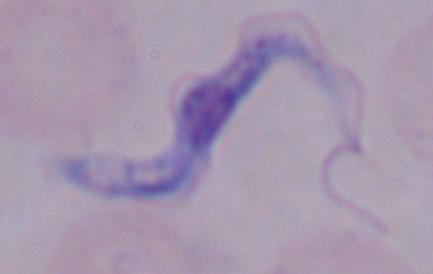

identification = trypanosome
magnification = 1000x
modality = photomicrograph